Name the parasite shown.
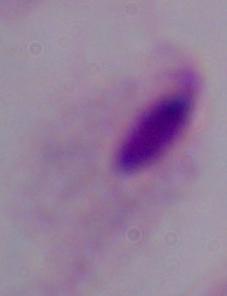

A trichomonad.

Summary:
  - Magnification: 1000x
  - Modality: micrograph